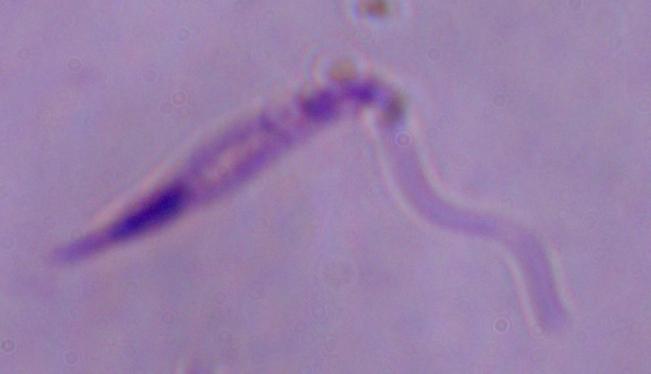 A Leishmania parasite is seen. Photomicrograph. Captured at 1000x magnification.